Name the cell type shown.
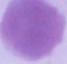

This is an erythrocyte.

Photomicrograph. 1000x magnification.